Name the parasite shown.
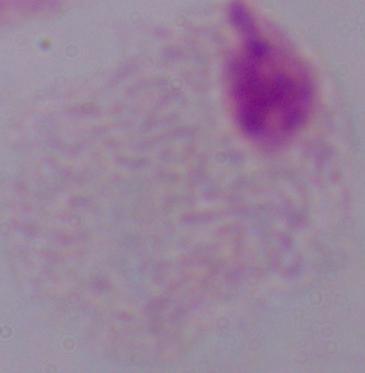
This is a trichomonad.

magnification = 1000x
modality = micrograph